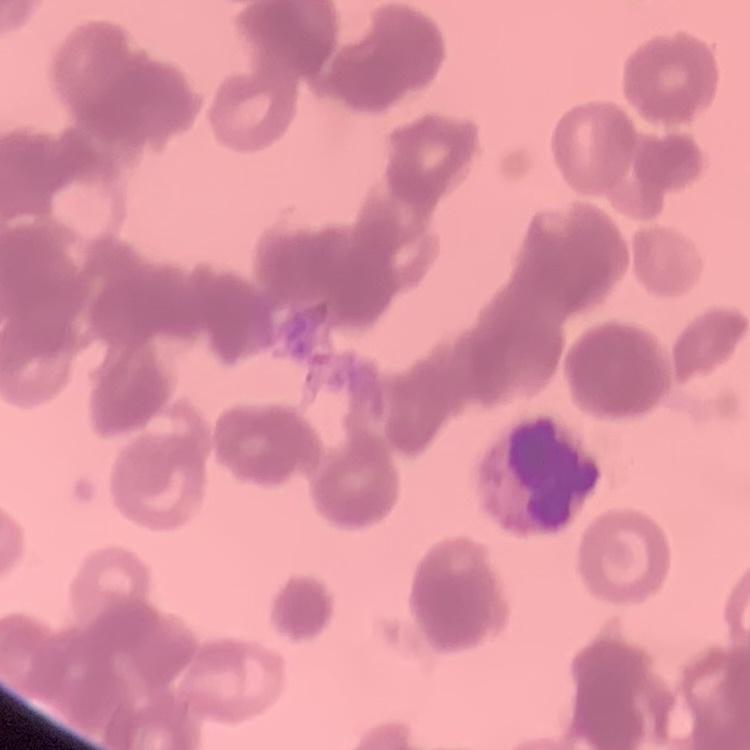 The red blood cells exhibit rouleaux formation. One tile cut from a larger photomicrograph. Thin peripheral smear. Stained with either Field's or Giemsa.